State which parasite is depicted.
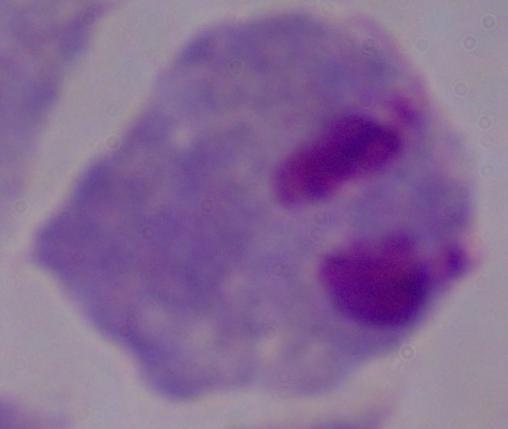

This is a trichomonad.

1000x magnification. Micrograph.